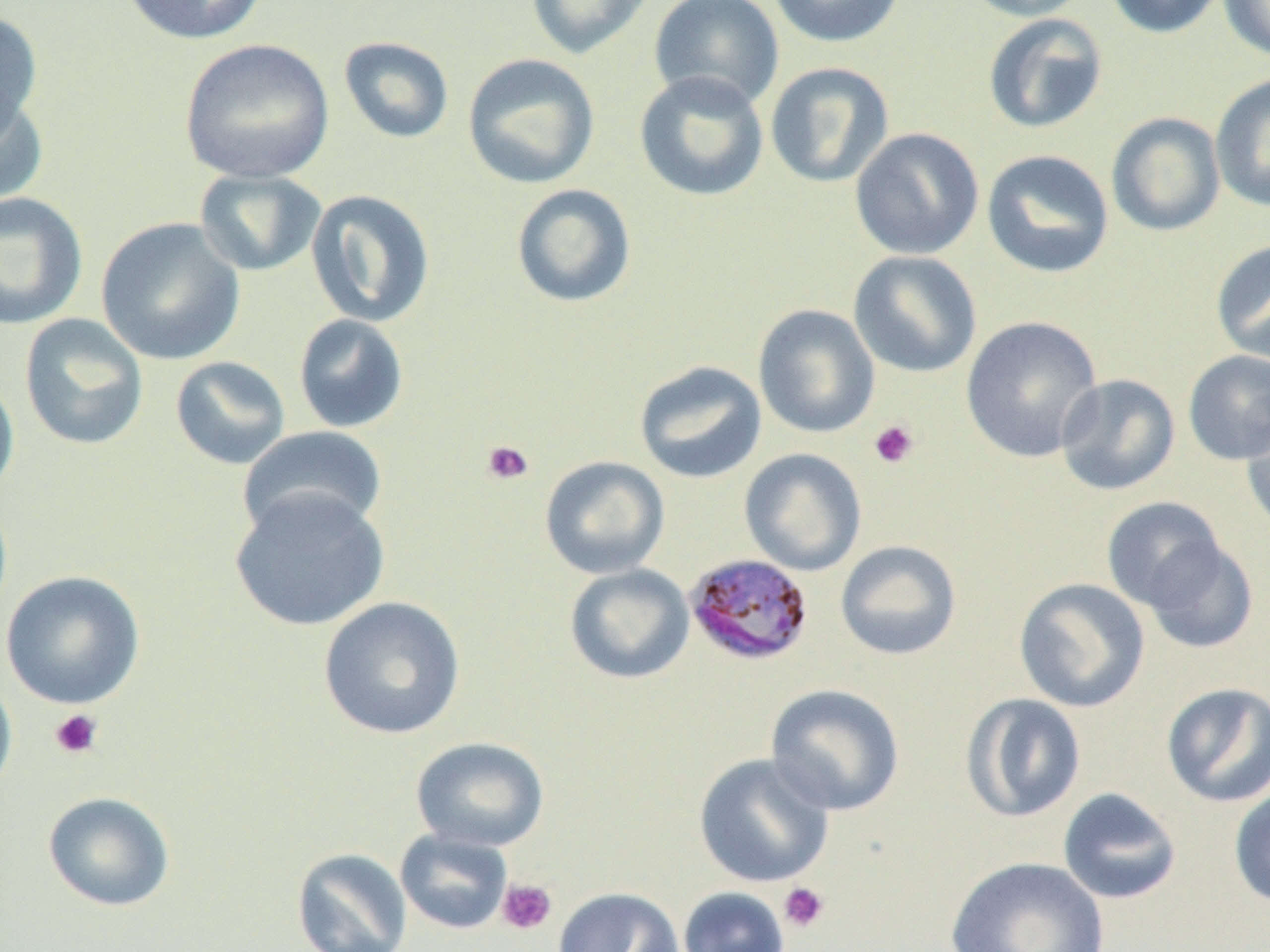
Summary:
  - Coordinate format: approximate bounding boxes as named x1/y1/x2/y2 corners in pixels
  - Plasmodium malariae-infected red blood cell locations: (x1=683, y1=552, x2=815, y2=667)
  - Uninfected red blood cell locations: (x1=120, y1=0, x2=267, y2=45), (x1=649, y1=0, x2=785, y2=111), (x1=767, y1=0, x2=906, y2=48), (x1=961, y1=0, x2=1092, y2=21), (x1=1102, y1=0, x2=1226, y2=39), (x1=1217, y1=0, x2=1270, y2=62), (x1=524, y1=1, x2=655, y2=60), (x1=0, y1=9, x2=44, y2=142), (x1=982, y1=13, x2=1109, y2=134), (x1=338, y1=36, x2=455, y2=144), (x1=179, y1=38, x2=334, y2=184), (x1=462, y1=53, x2=600, y2=190), (x1=765, y1=62, x2=895, y2=188), (x1=634, y1=70, x2=770, y2=202), (x1=1210, y1=73, x2=1270, y2=214), (x1=0, y1=87, x2=48, y2=208), (x1=1106, y1=112, x2=1226, y2=237), (x1=849, y1=127, x2=985, y2=260), (x1=981, y1=149, x2=1115, y2=279), (x1=194, y1=169, x2=328, y2=277), (x1=510, y1=184, x2=638, y2=309), (x1=305, y1=188, x2=436, y2=328), (x1=0, y1=192, x2=88, y2=330), (x1=96, y1=217, x2=246, y2=366), (x1=1210, y1=240, x2=1270, y2=364), (x1=848, y1=250, x2=982, y2=379), (x1=752, y1=304, x2=880, y2=438), (x1=19, y1=313, x2=149, y2=451), (x1=292, y1=313, x2=410, y2=434), (x1=960, y1=316, x2=1103, y2=462), (x1=1182, y1=349, x2=1270, y2=466), (x1=170, y1=355, x2=291, y2=470), (x1=634, y1=360, x2=767, y2=484), (x1=0, y1=368, x2=20, y2=503), (x1=1054, y1=373, x2=1181, y2=496), (x1=1241, y1=408, x2=1270, y2=538), (x1=238, y1=425, x2=387, y2=540), (x1=739, y1=448, x2=867, y2=577), (x1=540, y1=455, x2=670, y2=579), (x1=229, y1=488, x2=390, y2=632), (x1=1101, y1=497, x2=1228, y2=612), (x1=1141, y1=536, x2=1258, y2=654), (x1=835, y1=540, x2=962, y2=660), (x1=564, y1=563, x2=695, y2=685), (x1=1, y1=570, x2=146, y2=710), (x1=1013, y1=578, x2=1150, y2=713), (x1=318, y1=596, x2=466, y2=740), (x1=0, y1=668, x2=18, y2=801), (x1=1160, y1=681, x2=1270, y2=808), (x1=764, y1=683, x2=906, y2=817), (x1=962, y1=693, x2=1087, y2=822), (x1=410, y1=736, x2=549, y2=852), (x1=693, y1=752, x2=835, y2=888), (x1=1228, y1=781, x2=1270, y2=909), (x1=1057, y1=787, x2=1183, y2=905), (x1=42, y1=791, x2=176, y2=912), (x1=394, y1=828, x2=514, y2=935), (x1=292, y1=847, x2=413, y2=952), (x1=945, y1=855, x2=1110, y2=952), (x1=553, y1=886, x2=684, y2=952), (x1=677, y1=886, x2=790, y2=952)
  - Platelet locations: (x1=869, y1=419, x2=919, y2=469), (x1=480, y1=439, x2=534, y2=486), (x1=49, y1=709, x2=104, y2=759), (x1=497, y1=879, x2=557, y2=934), (x1=778, y1=882, x2=830, y2=933)
  - Slide-level diagnosis: Plasmodium malariae
  - Magnification: 1000x
  - Field of view: one of a larger specimen
  - Modality: light microscopy
  - Image size: 1270×952 pixels
  - Preparation: thin blood smear